Name the blood parasite species.
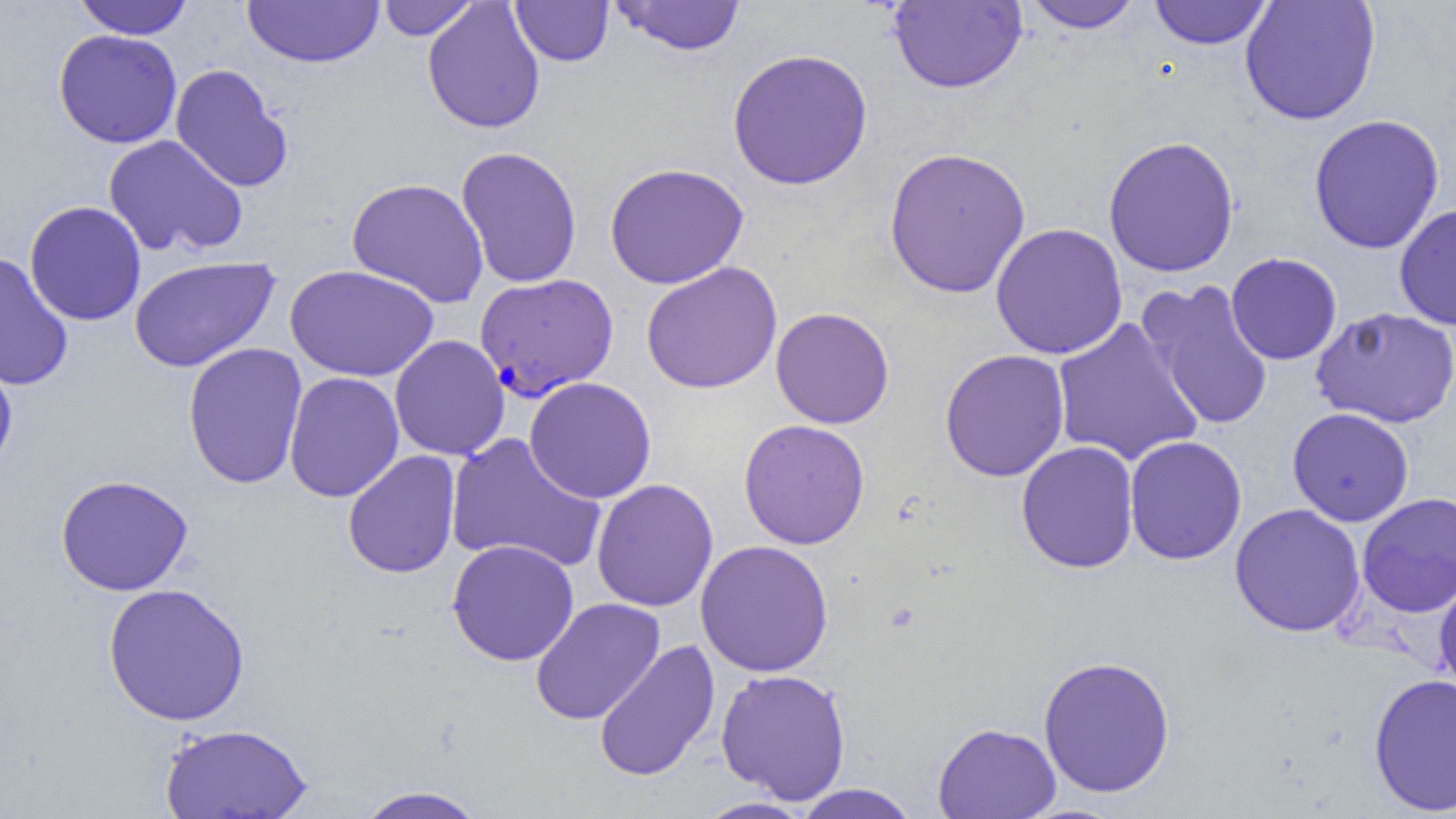
Plasmodium falciparum.

Approximate bounding boxes as [x1, y1, x2, y2] in pixels. Uninfected red blood cell locations (subset): [72, 0, 194, 39], [242, 0, 383, 68], [376, 0, 480, 41], [510, 0, 614, 67], [611, 0, 746, 56], [1240, 0, 1381, 125], [422, 1, 545, 134], [889, 1, 1026, 94], [1022, 1, 1144, 33], [1148, 1, 1274, 49], [53, 29, 182, 149], [726, 47, 873, 190], [169, 64, 294, 193], [1308, 113, 1445, 255], [103, 134, 249, 258], [1103, 135, 1240, 278], [455, 146, 583, 289], [883, 146, 1032, 299], [604, 162, 749, 290], [346, 177, 489, 308], [24, 200, 147, 326], [1394, 203, 1456, 330], [990, 222, 1128, 360], [1225, 252, 1343, 365], [0, 253, 73, 390], [129, 256, 281, 372], [641, 261, 782, 394], [285, 265, 439, 382], [1138, 279, 1275, 432], [1312, 306, 1456, 428], [770, 307, 895, 429], [1052, 318, 1204, 467], [389, 334, 510, 461], [182, 342, 308, 489], [939, 349, 1071, 482], [0, 350, 18, 476], [283, 371, 404, 502], [524, 376, 657, 504], [1286, 407, 1414, 527], [738, 419, 870, 550], [445, 432, 606, 573], [1124, 435, 1247, 565], [1015, 440, 1140, 574], [342, 450, 461, 578], [55, 474, 193, 596], [591, 478, 719, 612], [1357, 492, 1456, 618], [1229, 503, 1366, 637], [446, 539, 580, 667], [695, 539, 834, 677], [102, 582, 250, 726], [530, 597, 665, 725], [593, 638, 720, 783], [1037, 655, 1176, 798], [715, 668, 852, 804], [1368, 672, 1456, 815], [158, 722, 314, 819], [932, 722, 1061, 819], [791, 784, 921, 818], [353, 785, 489, 819], [693, 797, 815, 818]. Plasmodium falciparum-infected red blood cell locations (subset): [474, 273, 618, 400]. Single field of view. Optical microscopy. Captured at 1000x magnification. Thin blood smear. Image is 1456×819 pixels.